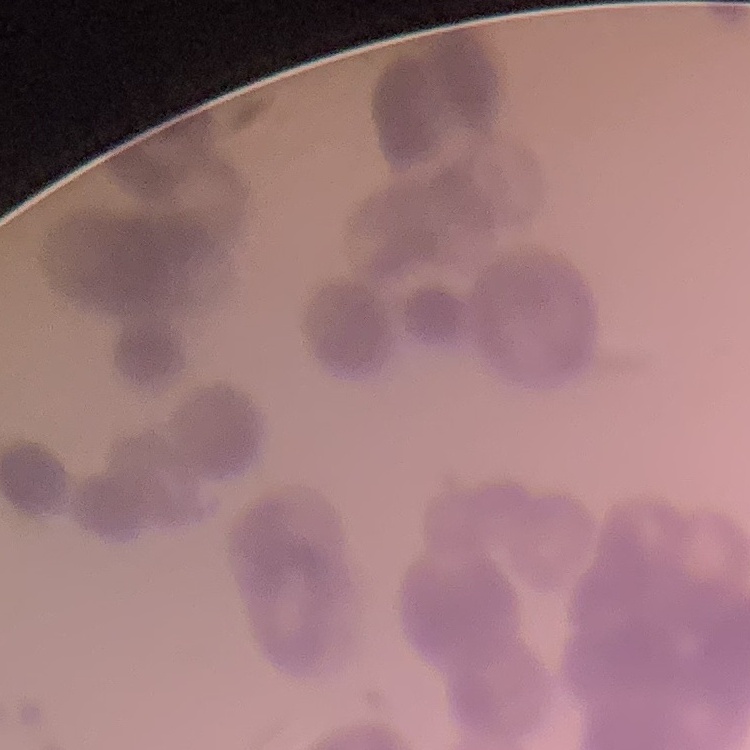

Summary:
  - Erythrocyte morphology: rouleaux formation
  - Stain: Field's or Giemsa
  - Image type: one tile cut from a larger photomicrograph
  - Preparation: thin blood smear